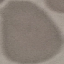
result = no malaria parasites seen
capture = smartphone camera at the microscope eyepiece
image type = automatically extracted cell patch, resized to 64 × 64 pixels
stain = Giemsa
preparation = thin blood smear